Name the parasite shown.
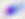

Toxoplasma gondii.

Captured at 400x magnification. Micrograph.